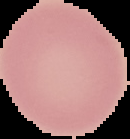

Summary:
  - Result: no malaria parasites seen
  - Image size: 130×139 pixels
  - Image type: segmented cell region on a black background
  - Preparation: thin blood smear